Name the parasite shown.
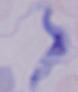

A trypanosome.

Summary:
  - Modality: photomicrograph
  - Magnification: 1000x